Classify this cell by malaria status.
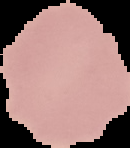
Uninfected.

{
  "preparation": "thin blood film",
  "image_size": "130×148 pixels",
  "image_type": "cell region segmented out of the field of view; surrounding area masked to black"
}